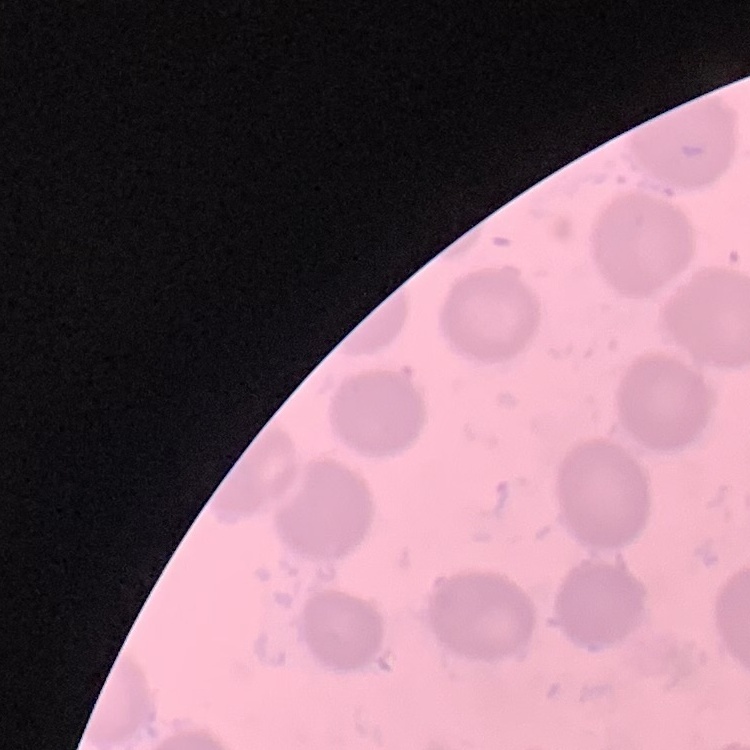

Summary:
  - Red blood cell morphology: no rouleaux formation
  - Preparation: thin blood film
  - Stain: Field's or Giemsa
  - Image type: square crop of a larger photomicrograph